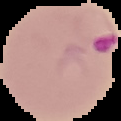
image_size: 121×121 pixels
image_type: segmented cell region with the area outside set to black
malaria_status: parasitized
preparation: thin blood smear